Mark where platelets are.
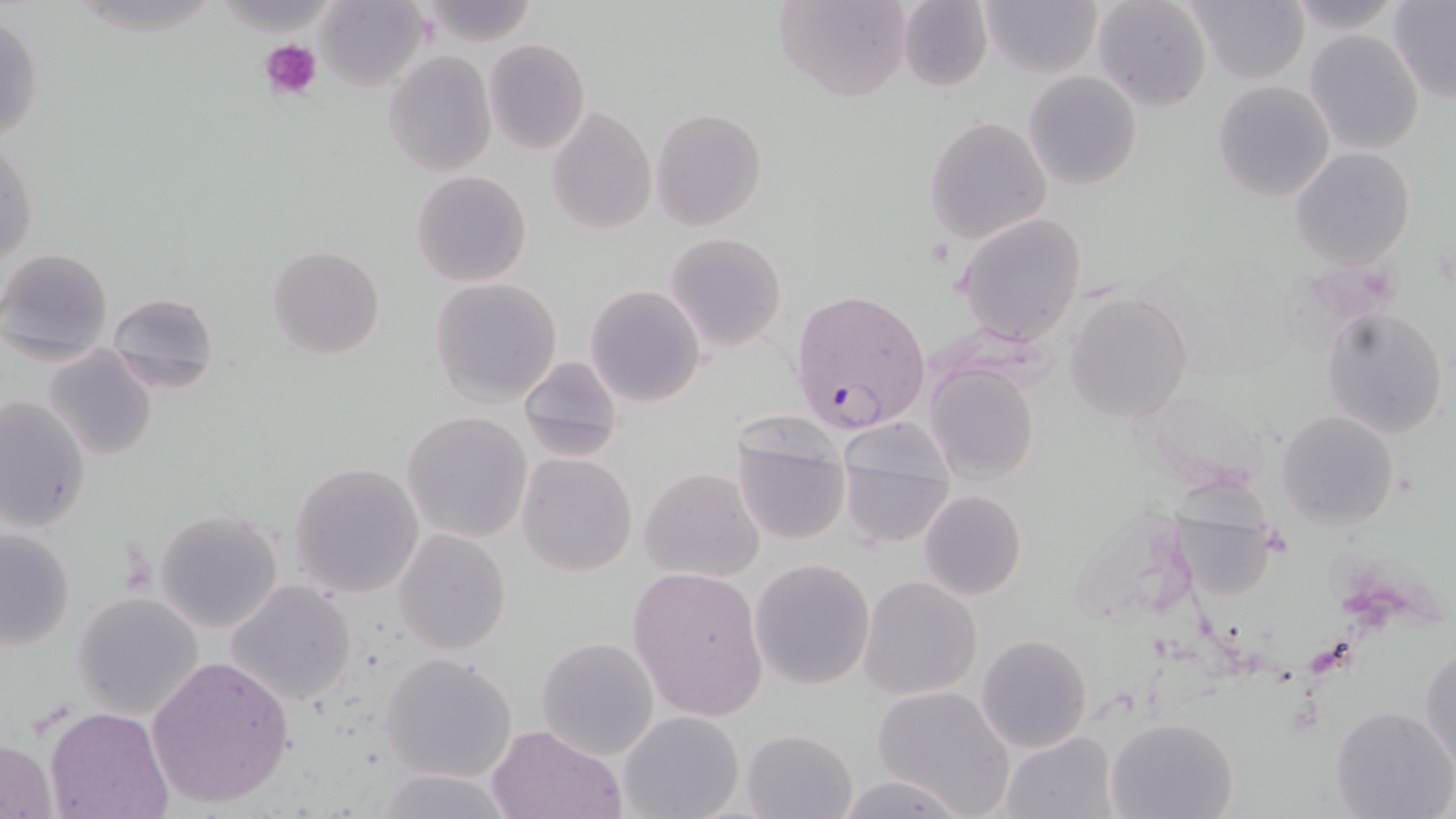

Approximate bounding boxes as [x1, y1, x2, y2] in pixels.
Platelets: [260, 39, 322, 102].

Plasmodium falciparum-infected red blood cell locations: [789, 290, 930, 434]. Uninfected red blood cell locations: [776, 0, 913, 102], [896, 0, 994, 93], [980, 0, 1103, 77], [1092, 0, 1213, 112], [316, 1, 428, 90], [417, 1, 542, 47], [1188, 1, 1308, 83], [1390, 1, 1456, 103], [1, 12, 44, 149], [1306, 30, 1424, 154], [484, 38, 589, 154], [383, 51, 496, 175], [1024, 72, 1141, 189], [1213, 80, 1335, 201], [547, 106, 656, 234], [650, 107, 768, 231], [924, 116, 1051, 244], [1, 137, 37, 269], [1290, 147, 1415, 268], [411, 169, 533, 288], [956, 213, 1088, 344], [664, 232, 786, 353], [267, 245, 387, 360], [0, 247, 114, 365], [430, 276, 563, 407], [585, 285, 706, 407], [106, 289, 220, 392], [1064, 292, 1194, 422], [1323, 306, 1448, 440], [43, 345, 159, 461], [516, 355, 624, 463], [925, 363, 1041, 484], [0, 395, 89, 534], [1277, 409, 1398, 530], [402, 410, 533, 542], [730, 422, 852, 548], [840, 440, 956, 550], [517, 453, 637, 576], [289, 462, 425, 599], [639, 467, 764, 583], [919, 489, 1026, 601], [1170, 505, 1279, 602], [155, 507, 284, 632], [0, 527, 76, 652], [393, 529, 511, 654], [750, 557, 876, 689], [627, 564, 771, 719], [860, 576, 981, 699], [226, 580, 358, 705], [72, 592, 205, 719], [976, 635, 1092, 753], [536, 637, 659, 759], [1421, 640, 1455, 771], [380, 650, 517, 782], [145, 653, 297, 808], [871, 686, 1017, 818], [1329, 705, 1454, 819], [45, 707, 174, 819], [620, 710, 744, 819], [1107, 715, 1238, 818], [486, 722, 627, 818], [741, 730, 856, 819], [1000, 730, 1120, 819], [1, 737, 58, 817], [371, 769, 516, 819], [833, 774, 967, 818]. Slide-level diagnosis: Plasmodium falciparum. Optical microscopy. Image is 1456×819 pixels. Captured at 1000x magnification. One field of a larger specimen. May-Grünwald-Giemsa-stained preparation. Thin blood smear.